Describe the morphology of the erythrocytes.
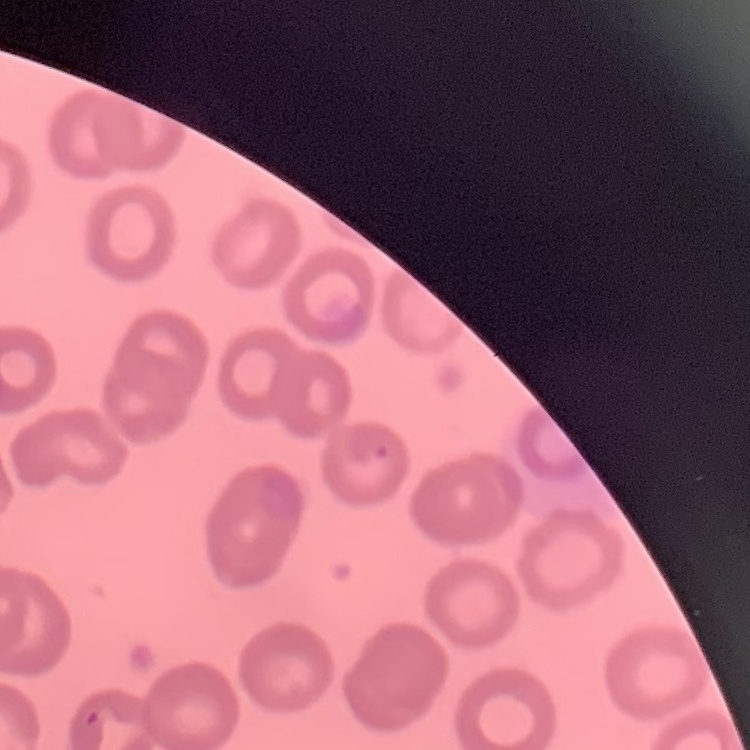

They show no rouleaux formation.

Field's or Giemsa stain. Thin blood smear. Square crop of a larger photomicrograph.